Classify this cell by malaria status.
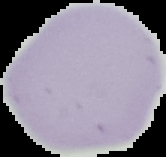

Uninfected.

image_type: segmented cell region on a black background
image_size: 166×157 pixels
preparation: thin blood film